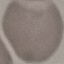

malaria status = uninfected
image type = cell patch, automatically extracted from a larger field of view and resized to 64 × 64 pixels
preparation = thin blood smear
capture = smartphone through the microscope eyepiece
stain = Giemsa